Locate every blood parasite and identify its species.
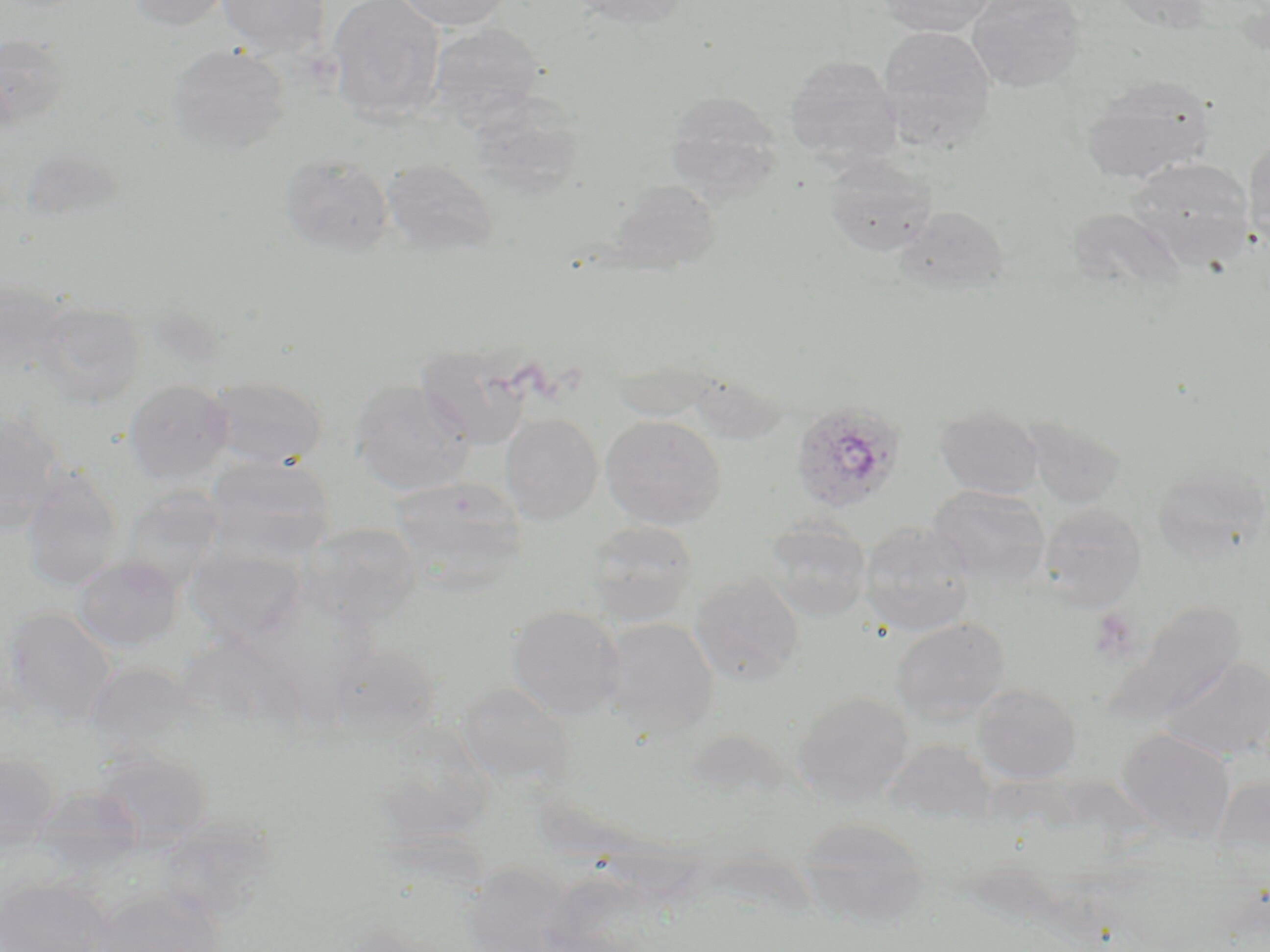

Approximate bounding boxes as (x1, y1, x2, y2) in pixels.
Plasmodium ovale-infected red blood cells: (789, 400, 906, 514).
No Plasmodium falciparum, Plasmodium malariae, Plasmodium vivax, Babesia divergens, or Trypanosoma brucei observed.

Summary:
  - Uninfected red blood cell locations: (125, 0, 234, 31), (217, 0, 330, 57), (328, 0, 445, 125), (395, 0, 514, 31), (564, 0, 693, 28), (878, 0, 997, 36), (968, 0, 1087, 92), (428, 22, 545, 128), (878, 25, 996, 153), (0, 34, 72, 128), (168, 43, 291, 156), (784, 54, 902, 166), (1080, 75, 1216, 184), (468, 89, 586, 198), (665, 91, 782, 199), (1244, 136, 1270, 247), (20, 147, 126, 225), (279, 154, 393, 257), (822, 155, 936, 256), (381, 158, 500, 258), (1126, 158, 1255, 266), (608, 180, 722, 274), (894, 205, 1010, 298), (1066, 208, 1187, 291), (0, 280, 72, 377), (32, 301, 145, 408), (416, 343, 533, 449), (205, 376, 327, 468), (350, 379, 474, 496), (125, 380, 233, 484), (935, 402, 1044, 499), (0, 411, 65, 531), (500, 413, 603, 525), (601, 414, 725, 529), (1022, 416, 1126, 509), (205, 454, 335, 559), (1152, 462, 1268, 560), (20, 465, 123, 590), (391, 476, 527, 581), (928, 485, 1049, 587), (121, 487, 227, 586), (1039, 502, 1146, 610), (581, 520, 700, 626), (299, 521, 422, 626), (764, 521, 872, 622), (858, 522, 975, 637), (186, 546, 306, 647), (73, 556, 183, 651), (689, 574, 805, 685), (1101, 603, 1245, 729), (506, 604, 627, 720), (1, 608, 117, 728), (890, 616, 1012, 723), (601, 617, 719, 737), (1159, 656, 1270, 761), (85, 663, 204, 759), (454, 681, 577, 791), (972, 683, 1082, 783), (792, 690, 914, 804), (1117, 727, 1235, 841), (91, 748, 213, 850), (0, 751, 60, 854), (1211, 775, 1270, 863), (33, 786, 142, 874), (797, 817, 931, 928), (0, 876, 108, 952), (90, 887, 226, 952)
  - Platelet locations: (1088, 608, 1140, 662)
  - Slide-level diagnosis: Plasmodium ovale
  - Field of view: one of a larger specimen
  - Stain: May-Grünwald-Giemsa
  - Preparation: thin blood film
  - Magnification: 1000x
  - Image size: 1270×952 pixels
  - Modality: light microscopy